Report the malaria status of this cell.
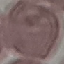
It is uninfected.

capture: smartphone camera at the microscope eyepiece
preparation: thin blood film
image_type: cell patch, automatically extracted from a larger field of view and resized to 64 × 64 pixels
stain: Giemsa